Describe the morphology of the erythrocytes.
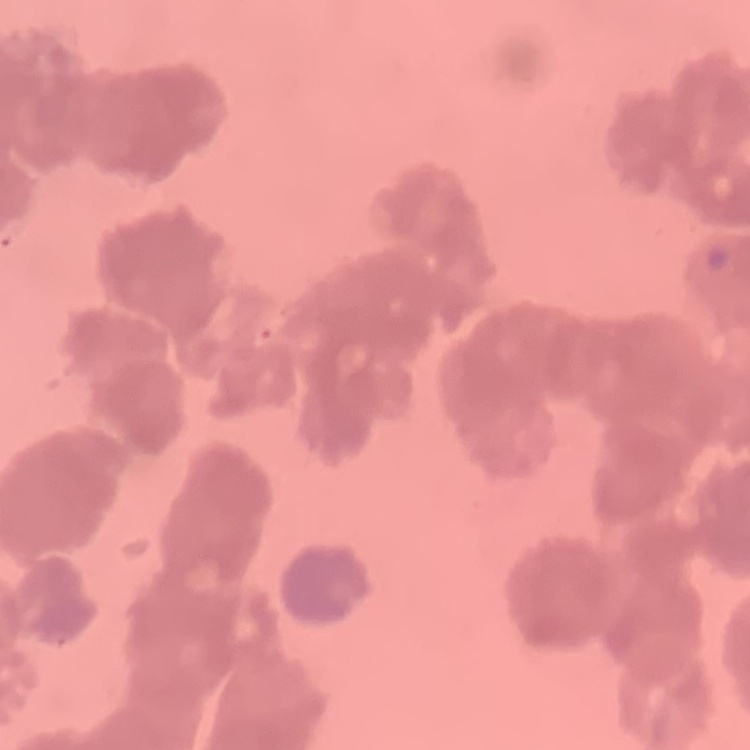
Rouleaux formation.

preparation = thin blood smear
stain = Field's or Giemsa
image type = square crop of a larger photomicrograph